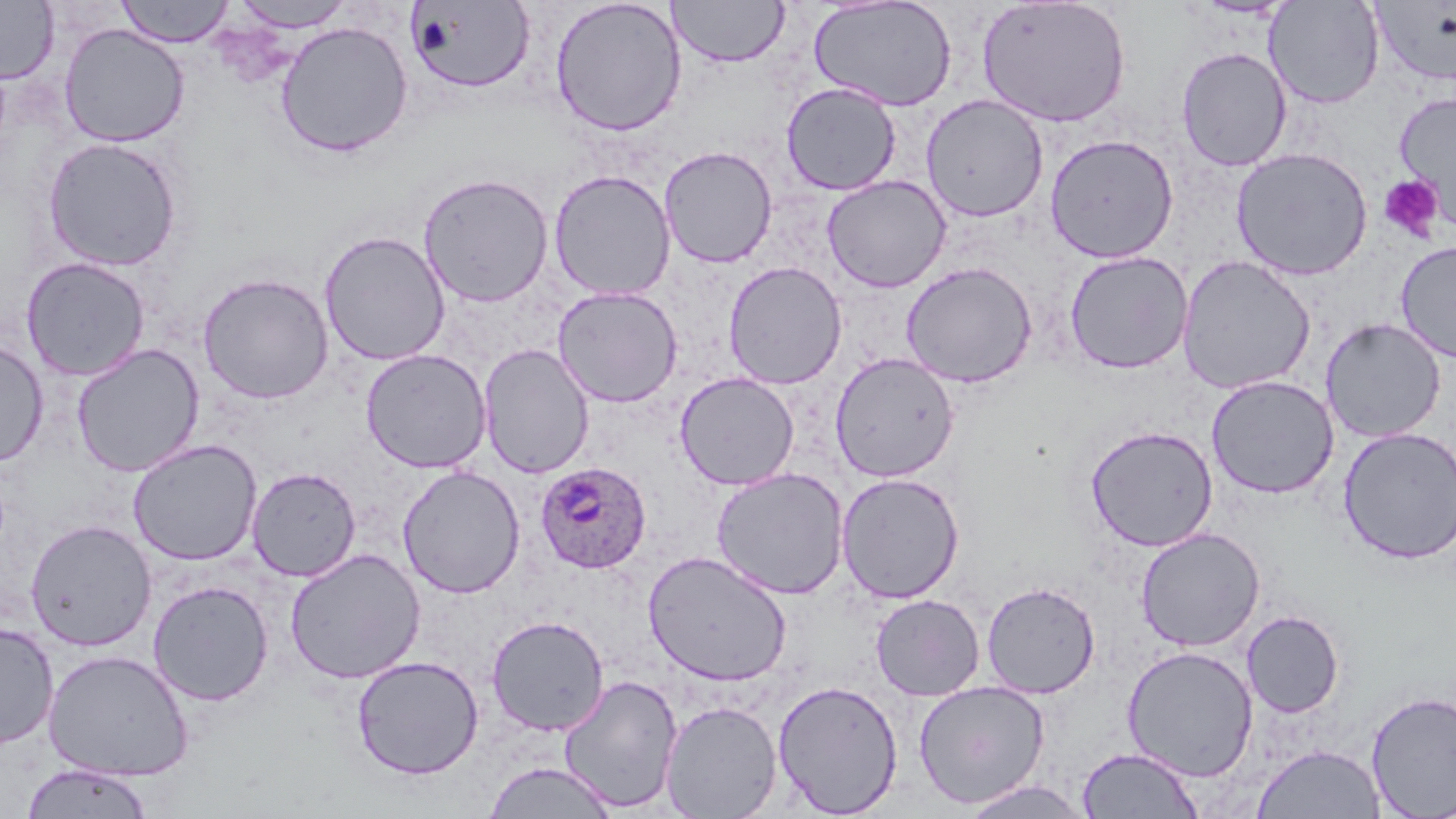
Approximate bounding boxes as (x1, y1, x2, y2) in pixels. Plasmodium ovale-infected red blood cell locations: (535, 461, 653, 574). Uninfected red blood cell locations: (115, 0, 236, 47), (549, 0, 687, 137), (667, 0, 789, 68), (809, 0, 957, 112), (0, 1, 59, 84), (231, 1, 356, 32), (406, 1, 535, 94), (976, 1, 1131, 128), (1263, 1, 1385, 109), (1371, 1, 1456, 88), (275, 21, 413, 158), (58, 23, 190, 147), (1176, 46, 1292, 171), (781, 82, 902, 196), (1393, 91, 1456, 225), (921, 94, 1049, 222), (1044, 133, 1179, 263), (41, 136, 184, 272), (659, 145, 778, 268), (1231, 147, 1373, 281), (548, 170, 677, 301), (418, 172, 554, 308), (821, 175, 951, 293), (318, 230, 451, 366), (1395, 241, 1456, 363), (1064, 251, 1193, 374), (1176, 255, 1316, 395), (21, 257, 149, 381), (723, 261, 847, 390), (900, 261, 1038, 388), (197, 272, 334, 404), (551, 286, 684, 408), (1320, 318, 1446, 443), (0, 338, 49, 467), (71, 343, 205, 477), (478, 344, 595, 479), (360, 348, 492, 473), (829, 352, 960, 482), (674, 372, 800, 490), (1205, 374, 1340, 499), (1084, 424, 1219, 551), (1337, 427, 1456, 564), (127, 439, 262, 566), (397, 465, 525, 599), (247, 466, 361, 582), (711, 467, 849, 600), (836, 472, 965, 603), (24, 518, 157, 651), (1136, 527, 1265, 652), (284, 548, 426, 684), (643, 550, 792, 686), (148, 579, 274, 706), (981, 581, 1101, 699), (870, 594, 985, 701), (1241, 610, 1344, 718), (486, 615, 610, 736), (0, 621, 59, 749), (1122, 645, 1259, 782), (43, 649, 195, 781), (351, 656, 484, 780), (558, 674, 684, 813), (772, 679, 904, 817), (913, 680, 1050, 809), (1365, 691, 1456, 817), (660, 700, 783, 818), (1252, 744, 1386, 818), (1076, 747, 1204, 818), (483, 760, 619, 818), (21, 762, 154, 819), (958, 779, 1094, 818). Platelet locations: (1378, 174, 1444, 242). Slide-level diagnosis: Plasmodium ovale. Single field of view. Thin blood film. Captured at 1000x magnification. Light microscopy. May-Grünwald-Giemsa stain. Image is 1456×819 pixels.